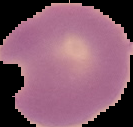

Summary:
  - Preparation: thin blood film
  - Result: Plasmodium parasites detected
  - Image type: segmented cell region on a black background
  - Image size: 133×127 pixels